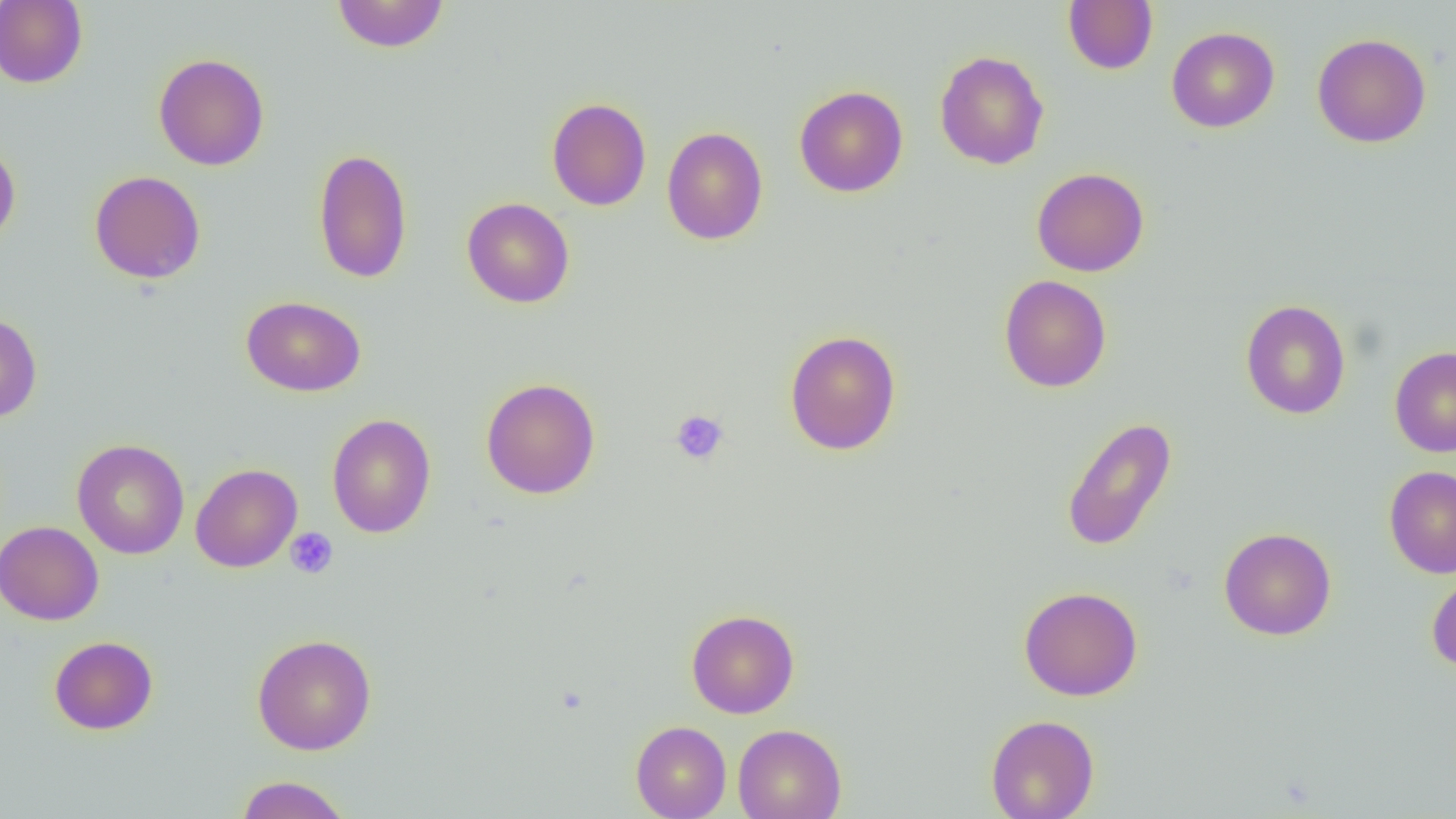
slide-level diagnosis = negative for blood parasites
platelet locations = approximate bounding boxes as [x1, y1, x2, y2] in pixels: [671, 409, 729, 464], [285, 527, 339, 579]
field of view = one of a larger specimen
uninfected red blood cell locations = approximate bounding boxes as [x1, y1, x2, y2] in pixels: [0, 0, 88, 88], [331, 0, 450, 53], [1062, 1, 1158, 74], [1166, 27, 1279, 132], [1312, 33, 1431, 148], [934, 50, 1049, 170], [154, 53, 270, 170], [794, 85, 908, 197], [547, 97, 652, 211], [661, 126, 768, 245], [0, 142, 20, 250], [313, 147, 413, 284], [1031, 167, 1149, 277], [89, 170, 206, 283], [461, 197, 575, 308], [999, 275, 1112, 393], [241, 295, 366, 396], [1240, 299, 1351, 419], [0, 312, 42, 422], [784, 329, 902, 455], [1390, 346, 1456, 457], [481, 378, 600, 499], [327, 413, 436, 538], [1061, 416, 1177, 552], [72, 439, 189, 560], [190, 463, 302, 572], [1384, 465, 1456, 579], [0, 521, 103, 625], [1219, 527, 1336, 640], [1426, 568, 1456, 673], [1019, 586, 1143, 701], [686, 609, 799, 718], [251, 633, 377, 755], [49, 636, 158, 735], [986, 714, 1100, 819], [630, 720, 731, 819], [733, 724, 847, 819], [234, 775, 352, 819]
preparation = thin blood smear
image size = 1456×819 pixels
modality = light microscopy
magnification = 1000x